Locate and identify every blood parasite.
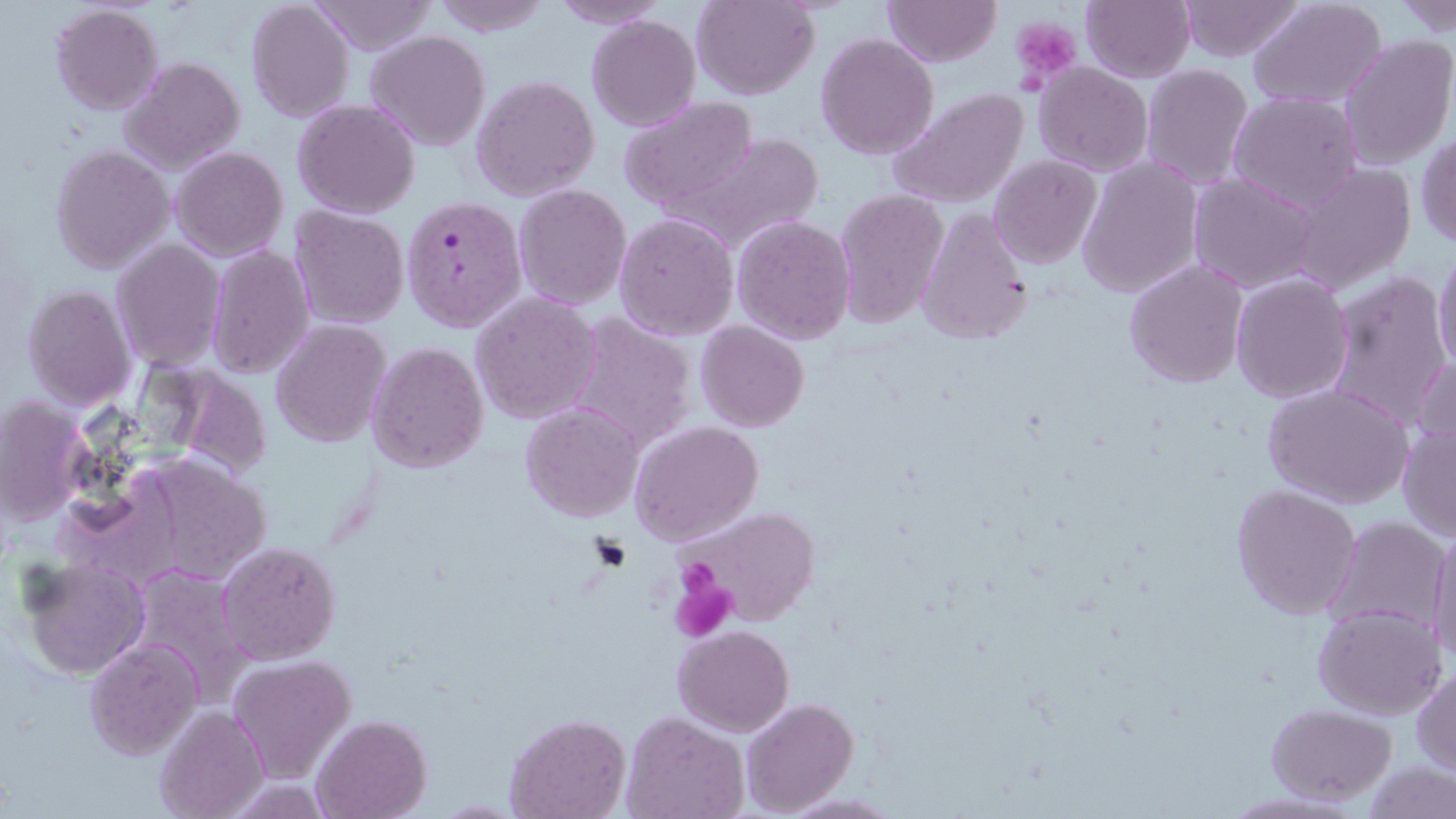
Approximate bounding boxes as (x1,y1)-(x2,y2) corner pairs in pixels.
Plasmodium falciparum-infected red blood cells: (403,198)-(525,332).
No Plasmodium ovale, Plasmodium malariae, Plasmodium vivax, Babesia divergens, or Trypanosoma brucei observed.

Summary:
  - Platelet locations: (1012,18)-(1082,84), (674,559)-(731,609), (670,575)-(738,641)
  - Uninfected red blood cell locations: (245,0)-(354,122), (309,0)-(438,55), (432,0)-(552,37), (690,0)-(820,100), (882,0)-(1001,67), (547,1)-(672,28), (1081,1)-(1195,81), (1177,1)-(1305,61), (1391,1)-(1455,39), (1249,2)-(1388,109), (50,3)-(162,115), (587,14)-(701,131), (366,30)-(490,151), (815,34)-(941,159), (1337,34)-(1455,174), (120,56)-(245,175), (1034,62)-(1153,175), (1140,65)-(1253,190), (472,75)-(600,202), (889,88)-(1029,209), (1228,92)-(1364,212), (616,98)-(758,213), (293,99)-(421,220), (1416,130)-(1456,251), (659,134)-(824,257), (51,144)-(173,273), (169,145)-(287,262), (990,156)-(1102,271), (1076,158)-(1203,298), (1285,164)-(1416,297), (1188,173)-(1322,293), (514,184)-(633,312), (834,190)-(950,330), (290,206)-(409,329), (915,210)-(1033,346), (614,213)-(739,341), (731,214)-(856,343), (112,240)-(224,370), (206,244)-(315,379), (1432,247)-(1456,378), (1124,260)-(1249,388), (1322,271)-(1453,434), (1231,273)-(1353,403), (22,285)-(133,410), (470,293)-(602,425), (562,313)-(697,455), (271,319)-(389,448), (696,321)-(810,434), (368,341)-(489,473), (1410,356)-(1456,468), (1263,383)-(1414,510), (0,396)-(92,525), (521,404)-(642,522), (629,420)-(764,548), (1396,421)-(1456,541), (116,449)-(276,589), (1230,484)-(1362,619), (670,503)-(821,632), (1327,516)-(1452,635), (1427,528)-(1456,664), (217,542)-(341,663), (22,557)-(149,679), (126,566)-(254,706), (1312,602)-(1445,719), (673,625)-(794,735), (83,636)-(201,760), (227,655)-(357,782), (1412,666)-(1456,776), (740,697)-(859,816), (1266,703)-(1397,803), (155,705)-(268,819), (621,711)-(750,819), (311,713)-(433,818), (503,713)-(630,819), (1361,761)-(1454,818), (221,777)-(337,816)
  - Slide-level diagnosis: Plasmodium falciparum
  - Magnification: 1000x
  - Stain: May-Grünwald-Giemsa
  - Modality: optical microscopy
  - Preparation: thin blood smear
  - Field of view: one of a larger specimen
  - Image size: 1456×819 pixels